Locate and identify every blood parasite.
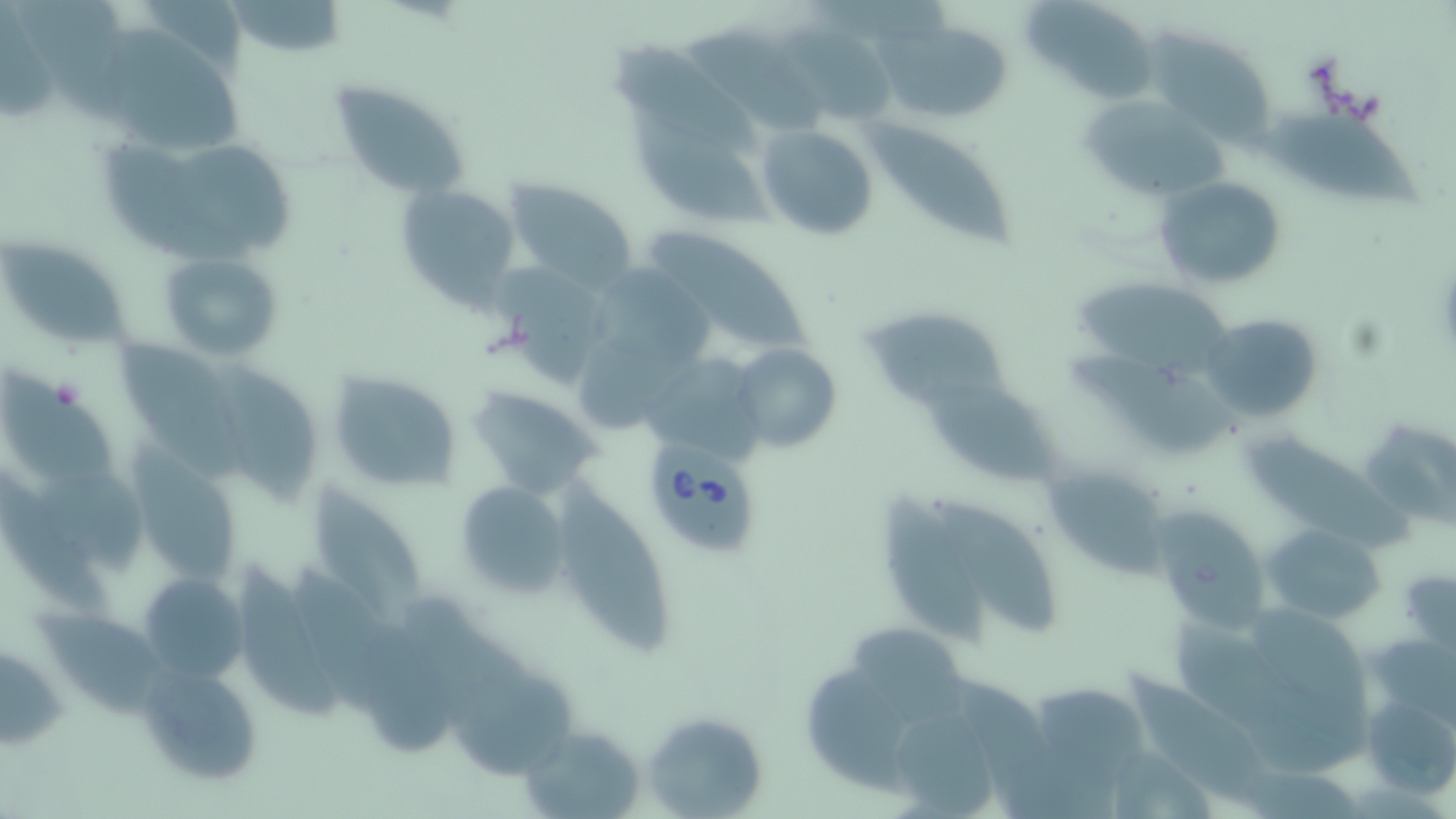
Approximate bounding boxes as named x1/y1/x2/y2 corners in pixels.
Babesia divergens-infected red blood cells: (x1=646, y1=447, x2=763, y2=557).
No Plasmodium falciparum, Plasmodium ovale, Plasmodium malariae, Plasmodium vivax, or Trypanosoma brucei observed.

Uninfected red blood cell locations: (x1=12, y1=1, x2=138, y2=124), (x1=227, y1=1, x2=349, y2=56), (x1=1025, y1=5, x2=1161, y2=103), (x1=872, y1=23, x2=1011, y2=120), (x1=785, y1=24, x2=899, y2=126), (x1=686, y1=25, x2=825, y2=132), (x1=1143, y1=30, x2=1276, y2=151), (x1=103, y1=31, x2=255, y2=152), (x1=610, y1=41, x2=767, y2=160), (x1=329, y1=80, x2=471, y2=201), (x1=1080, y1=96, x2=1231, y2=201), (x1=1265, y1=105, x2=1423, y2=213), (x1=636, y1=112, x2=769, y2=228), (x1=870, y1=121, x2=1013, y2=248), (x1=758, y1=125, x2=877, y2=240), (x1=100, y1=139, x2=262, y2=264), (x1=183, y1=144, x2=302, y2=250), (x1=1154, y1=175, x2=1287, y2=292), (x1=505, y1=178, x2=636, y2=286), (x1=395, y1=180, x2=523, y2=309), (x1=643, y1=227, x2=813, y2=355), (x1=2, y1=236, x2=127, y2=351), (x1=158, y1=250, x2=283, y2=361), (x1=497, y1=267, x2=624, y2=386), (x1=1080, y1=278, x2=1229, y2=373), (x1=1201, y1=313, x2=1322, y2=423), (x1=862, y1=315, x2=1012, y2=408), (x1=115, y1=340, x2=228, y2=447), (x1=730, y1=343, x2=843, y2=453), (x1=1071, y1=349, x2=1253, y2=452), (x1=646, y1=361, x2=762, y2=456), (x1=2, y1=363, x2=118, y2=491), (x1=218, y1=366, x2=317, y2=502), (x1=327, y1=370, x2=461, y2=494), (x1=925, y1=380, x2=1053, y2=487), (x1=468, y1=386, x2=601, y2=499), (x1=1362, y1=418, x2=1454, y2=527), (x1=1254, y1=432, x2=1417, y2=550), (x1=133, y1=460, x2=243, y2=587), (x1=1046, y1=466, x2=1173, y2=581), (x1=41, y1=472, x2=145, y2=580), (x1=454, y1=479, x2=570, y2=598), (x1=556, y1=480, x2=674, y2=658), (x1=313, y1=481, x2=423, y2=632), (x1=883, y1=495, x2=987, y2=648), (x1=936, y1=502, x2=1059, y2=633), (x1=1150, y1=505, x2=1268, y2=628), (x1=1263, y1=524, x2=1385, y2=623), (x1=234, y1=565, x2=342, y2=722), (x1=1398, y1=567, x2=1456, y2=659), (x1=139, y1=574, x2=247, y2=680), (x1=1173, y1=597, x2=1385, y2=778), (x1=32, y1=610, x2=178, y2=728), (x1=860, y1=627, x2=966, y2=721), (x1=0, y1=643, x2=68, y2=750), (x1=802, y1=661, x2=904, y2=792), (x1=144, y1=665, x2=261, y2=786), (x1=1130, y1=668, x2=1278, y2=804), (x1=452, y1=669, x2=583, y2=775), (x1=1033, y1=683, x2=1151, y2=782), (x1=1358, y1=686, x2=1456, y2=803), (x1=642, y1=708, x2=768, y2=818), (x1=894, y1=708, x2=999, y2=818), (x1=516, y1=722, x2=646, y2=819). Slide-level diagnosis: Babesia divergens. Image is 1456×819 pixels. Thin blood smear. Light microscopy. May-Grünwald-Giemsa-stained preparation. One field of a larger specimen. Captured at 1000x magnification.